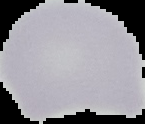
From a thin blood film. Image is 145×124 pixels. Malaria status: uninfected. The area outside the segmented cell region is set to black.